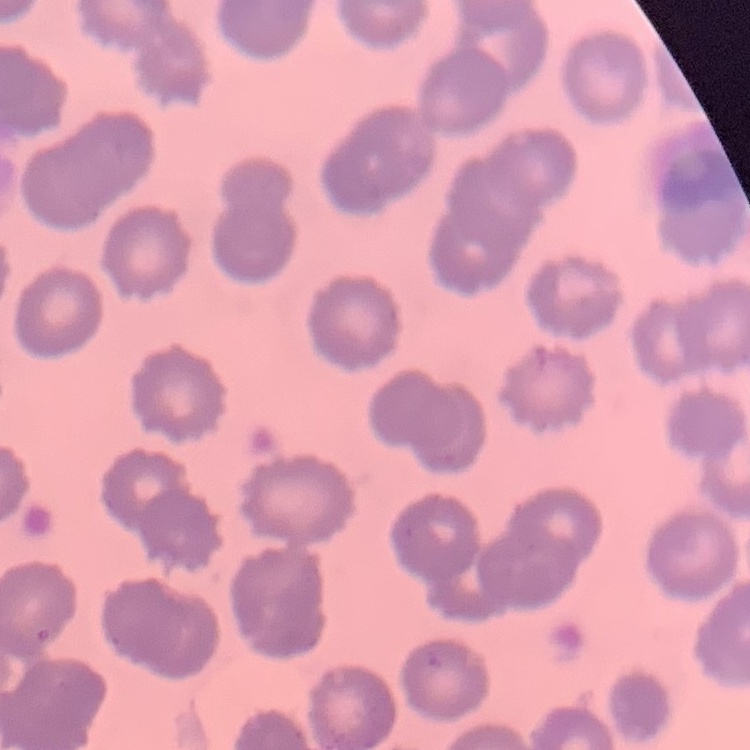 The erythrocytes show no rouleaux formation. One tile cut from a larger photomicrograph. Field's or Giemsa stain. Thin peripheral smear.